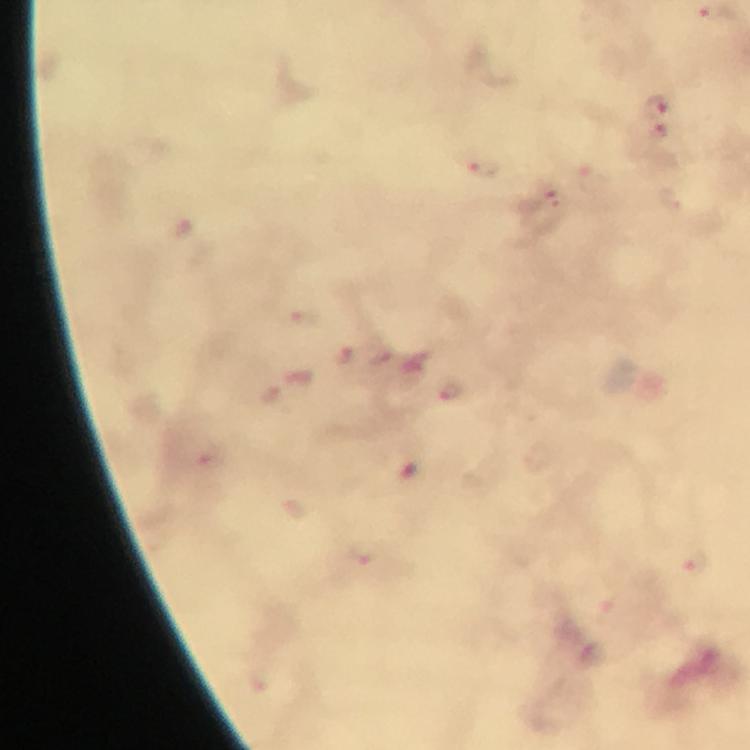

Approximate centers as (x, y) in pixels.
Summary:
  - Plasmodium parasite locations: (714, 11), (656, 103), (658, 131), (481, 168), (551, 202), (341, 356), (452, 390), (693, 561)
  - Image size: 750×750 pixels
  - Context: from a malaria diagnostic workup
  - Immersion oil: used
  - Cropped from: a single field of view
  - Capture: smartphone photograph through a microscope
  - Stain: Giemsa
  - Preparation: thick blood film
  - Magnification: 100x